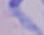

magnification: 1000x
identification: trypanosome
modality: micrograph